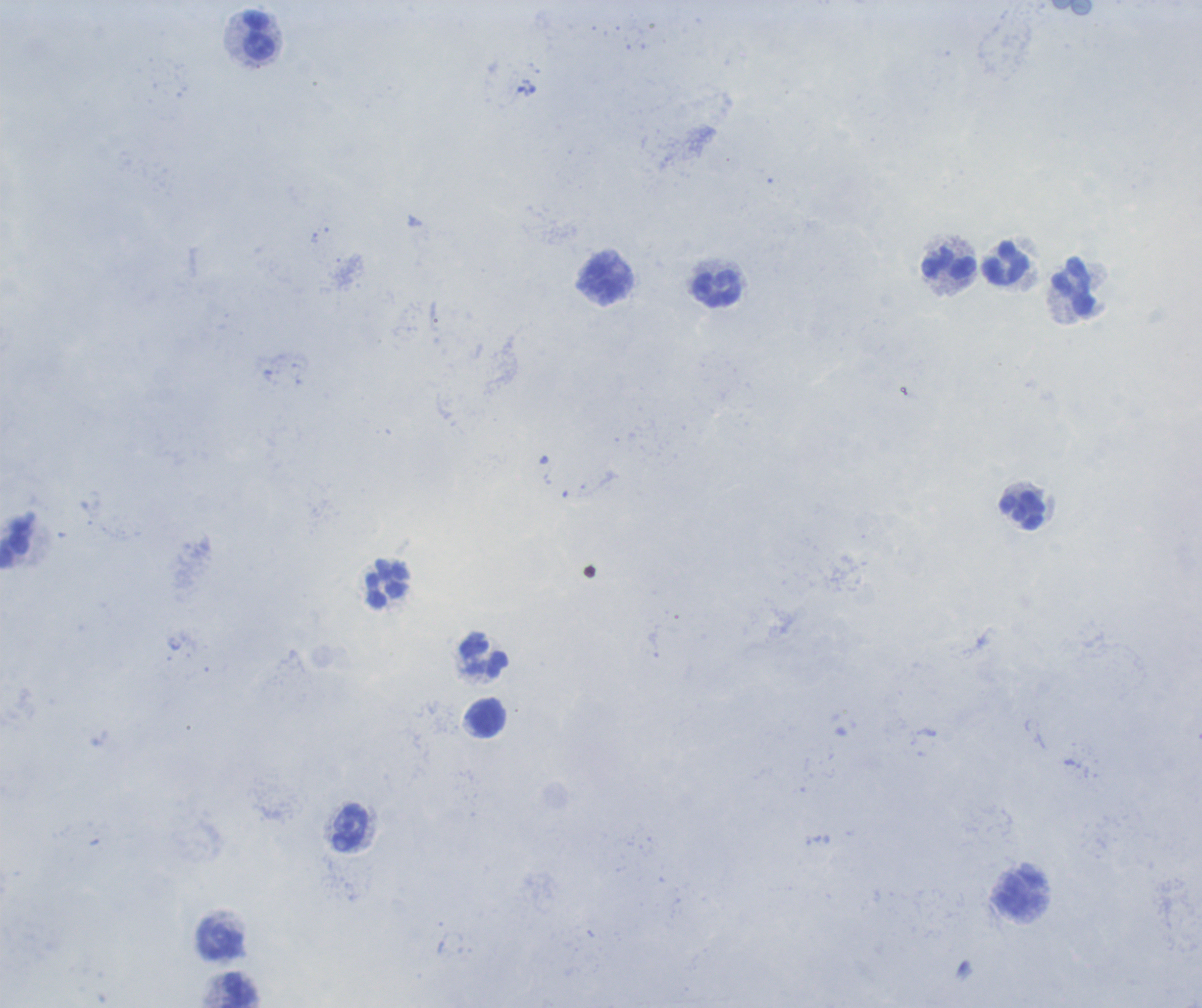
coordinate format = approximate centers as {x, y} in pixels
leukocyte locations = {258, 35}, {951, 266}, {1005, 266}, {606, 280}, {1073, 288}, {717, 290}, {1022, 511}, {15, 545}, {388, 584}, {484, 654}, {488, 719}, {349, 826}, {1023, 895}, {222, 939}, {239, 990}
background quality = unsatisfactory
magnification = 100x
context = previously used in a real diagnosis
field of view = single
result = no malaria parasites detected
image size = 1202×1008 pixels
preparation = thick blood smear
stain = Romanowsky